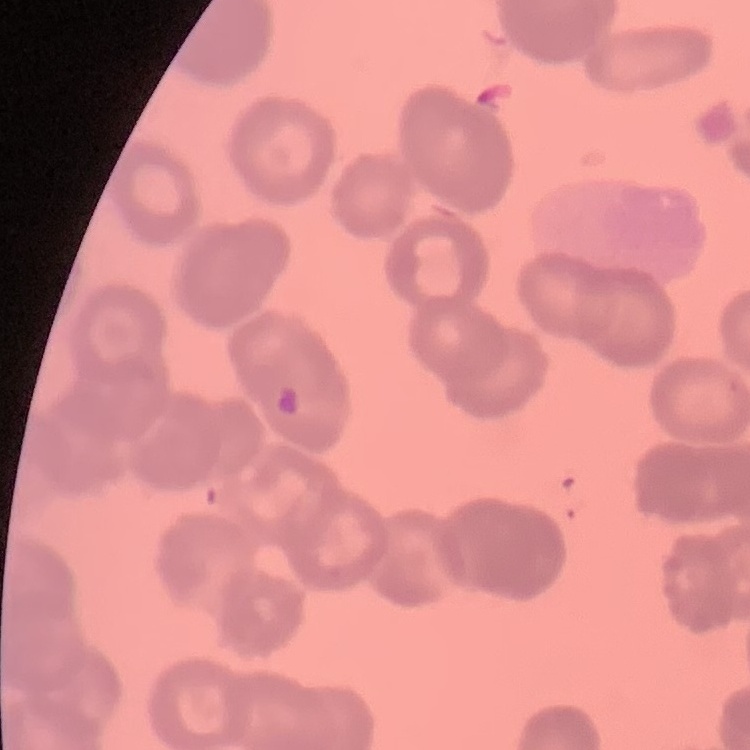
erythrocyte morphology = rouleaux formation
preparation = thin peripheral smear
image type = one tile cut from a larger photomicrograph
stain = Field's or Giemsa